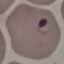
Summary:
  - Malaria status: parasitized
  - Stain: Giemsa
  - Image type: cell patch, automatically extracted from a larger field of view and resized to 64 × 64 pixels
  - Preparation: thin blood film
  - Capture: smartphone camera at the microscope eyepiece